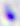

modality: micrograph
magnification: 400x
identification: Toxoplasma gondii